Report the malaria status of this cell.
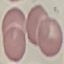
It is uninfected.

Photographed with a smartphone camera at the microscope eyepiece. Thin blood smear. Giemsa-stained preparation. Automatically extracted cell patch, resized to 64 × 64 pixels.